Name the parasite shown.
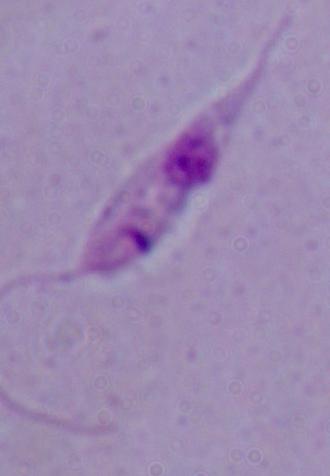

This is Leishmania.

Summary:
  - Modality: photomicrograph
  - Magnification: 1000x